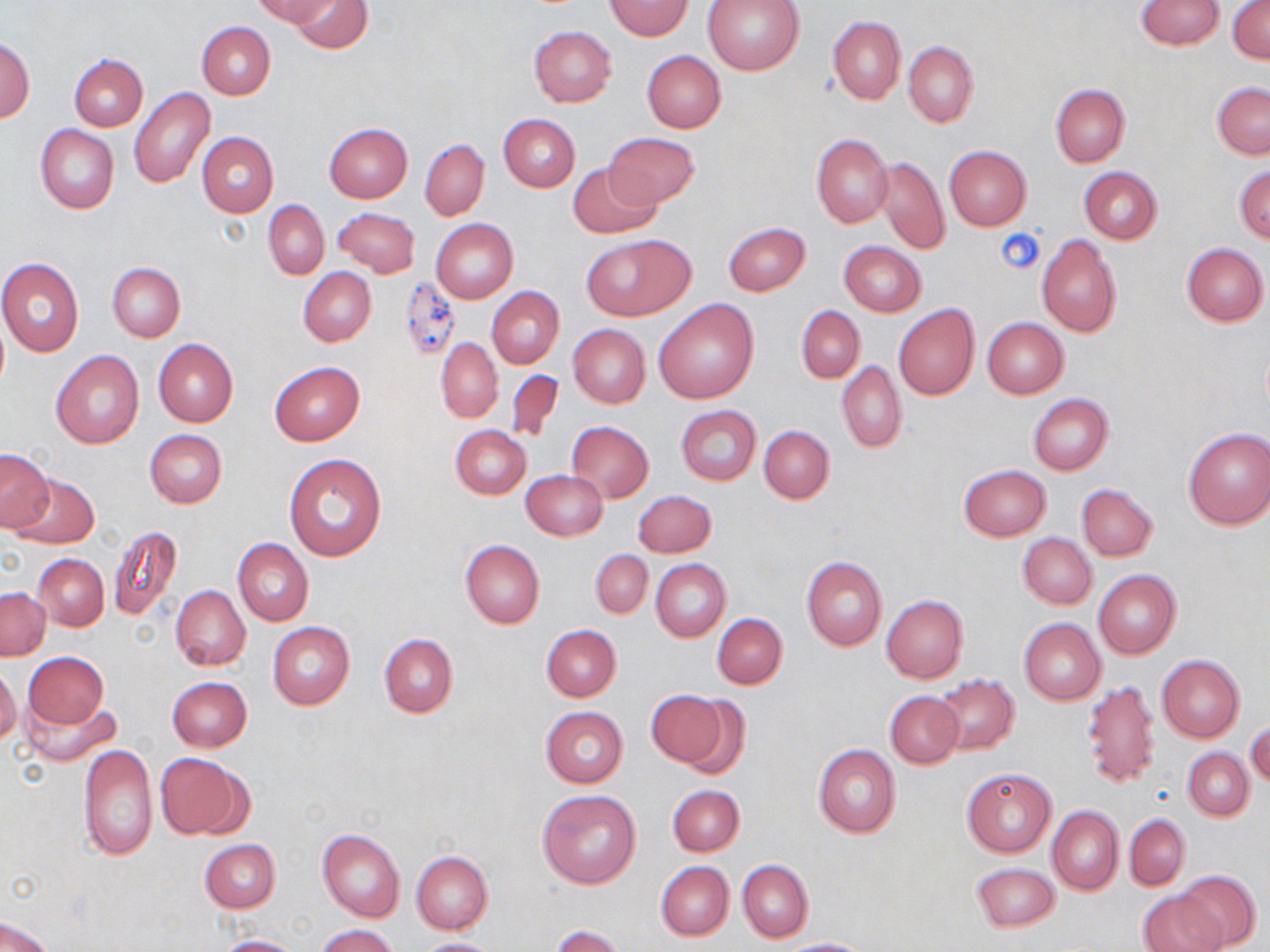

Summary:
  - Coordinate format: approximate bounding boxes as (x1, y1, x2, y2) in pixels
  - Uninfected red blood cell locations: (253, 0, 339, 26), (288, 0, 372, 53), (702, 0, 804, 75), (1135, 0, 1225, 49), (604, 1, 692, 40), (1229, 2, 1270, 64), (827, 15, 906, 104), (196, 21, 275, 99), (529, 26, 616, 107), (1, 38, 34, 123), (904, 41, 978, 128), (641, 50, 726, 133), (69, 53, 147, 130), (1212, 82, 1270, 159), (1051, 84, 1130, 167), (129, 88, 215, 189), (498, 114, 580, 191), (35, 123, 119, 214), (324, 123, 412, 201), (197, 132, 278, 216), (604, 132, 699, 209), (812, 133, 893, 227), (420, 139, 489, 220), (944, 145, 1031, 230), (872, 157, 949, 255), (568, 162, 660, 240), (1234, 164, 1270, 244), (1078, 166, 1162, 244), (263, 200, 329, 279), (333, 207, 420, 278), (431, 218, 518, 303), (722, 221, 810, 296), (580, 234, 695, 321), (1035, 234, 1121, 337), (838, 240, 927, 316), (1182, 243, 1268, 326), (0, 258, 85, 356), (108, 263, 186, 343), (298, 267, 376, 346), (487, 286, 564, 368), (654, 298, 759, 405), (893, 304, 979, 400), (796, 306, 865, 383), (982, 317, 1069, 398), (569, 324, 650, 408), (153, 338, 237, 428), (436, 338, 503, 423), (51, 351, 144, 449), (836, 360, 906, 453), (269, 362, 364, 446), (506, 370, 564, 444), (1027, 393, 1113, 475), (675, 405, 761, 484), (567, 421, 653, 503), (450, 425, 531, 500), (759, 426, 834, 503), (1183, 427, 1270, 530), (144, 429, 227, 507), (0, 448, 54, 532), (284, 453, 387, 560), (958, 465, 1052, 541), (520, 470, 607, 539), (11, 474, 99, 549), (1077, 483, 1157, 562), (632, 490, 716, 558), (107, 525, 182, 621), (1017, 532, 1096, 609), (233, 538, 314, 626), (460, 540, 544, 629), (590, 549, 652, 619), (34, 553, 109, 630), (801, 556, 887, 650), (651, 559, 731, 642), (1093, 569, 1181, 658), (171, 585, 250, 670), (0, 588, 50, 659), (881, 594, 967, 683), (712, 613, 788, 690), (1018, 618, 1105, 705), (268, 621, 355, 708), (542, 624, 620, 701), (379, 632, 458, 717), (23, 651, 109, 729), (1156, 655, 1245, 743), (0, 666, 21, 745), (934, 674, 1019, 756), (168, 676, 252, 752), (1082, 678, 1161, 788), (646, 689, 735, 770), (885, 690, 963, 768), (21, 693, 120, 767), (540, 706, 629, 787), (1246, 722, 1269, 787), (79, 742, 156, 862), (812, 744, 901, 838), (1182, 748, 1253, 820), (157, 753, 246, 837), (961, 767, 1057, 857), (668, 785, 744, 856), (537, 789, 641, 888), (1047, 805, 1124, 894), (1125, 814, 1190, 890), (316, 829, 405, 923), (200, 839, 280, 913), (411, 851, 492, 934), (737, 859, 813, 942), (657, 862, 733, 941), (971, 863, 1060, 931), (1173, 870, 1262, 950), (1138, 891, 1226, 952), (0, 915, 55, 952), (316, 924, 398, 952), (552, 925, 624, 952), (214, 934, 304, 952), (413, 938, 503, 951), (781, 938, 870, 951)
  - Platelet locations: (997, 227, 1044, 276)
  - Slide-level diagnosis: no evidence of blood parasites
  - Field of view: single
  - Stain: May-Grünwald-Giemsa
  - Modality: light microscopy
  - Preparation: thin blood smear
  - Image size: 1270×952 pixels
  - Magnification: 1000x